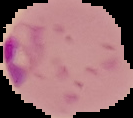
Summary:
  - Image size: 133×118 pixels
  - Malaria status: parasitized
  - Preparation: thin blood film
  - Image type: segmented cell region with the area outside set to black